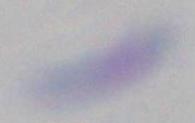

modality = micrograph
identification = Toxoplasma gondii
magnification = 1000x